Report the malaria status of this cell.
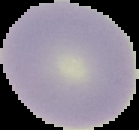

Uninfected.

image size = 139×130 pixels
preparation = thin blood smear
image type = segmented cell region on a black background